Locate every Plasmodium falciparum-infected red blood cell.
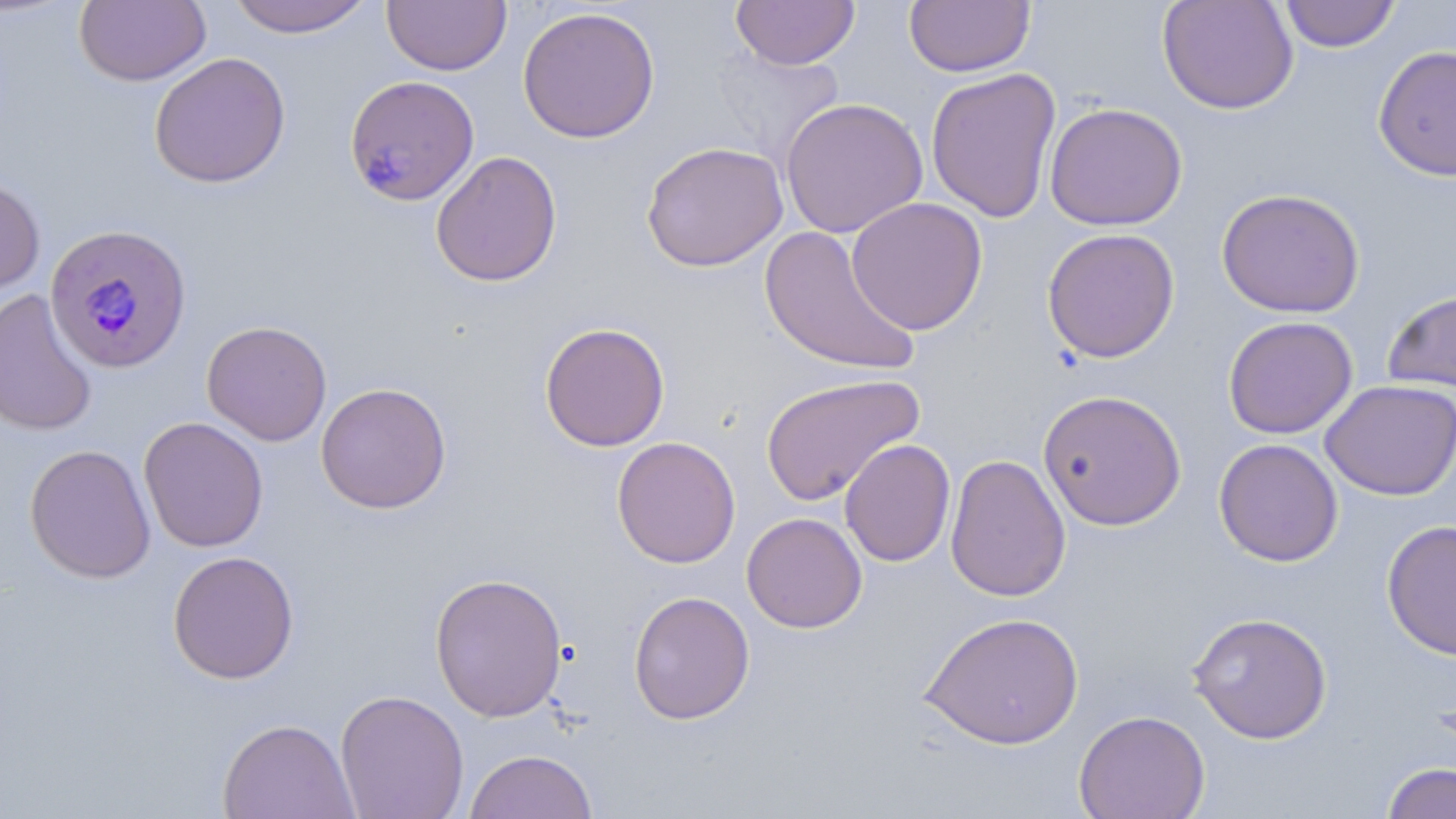
Approximate bounding boxes as (x1, y1, x2, y2) in pixels.
Plasmodium falciparum-infected red blood cells: (344, 75, 480, 206), (42, 225, 190, 374).

Uninfected red blood cell locations: (74, 0, 212, 87), (226, 0, 375, 38), (382, 0, 511, 76), (730, 0, 860, 70), (1157, 0, 1299, 115), (1279, 0, 1401, 52), (904, 1, 1035, 77), (517, 6, 660, 144), (1373, 45, 1456, 181), (148, 52, 292, 188), (925, 66, 1062, 223), (779, 97, 928, 238), (1044, 102, 1188, 231), (641, 140, 789, 272), (430, 150, 563, 288), (0, 174, 46, 296), (1216, 187, 1366, 318), (846, 196, 988, 336), (759, 226, 921, 378), (1041, 228, 1180, 363), (1382, 286, 1456, 395), (0, 289, 99, 436), (1223, 315, 1358, 439), (201, 320, 333, 446), (539, 321, 671, 452), (760, 372, 925, 506), (1320, 379, 1456, 501), (316, 382, 452, 513), (1038, 389, 1187, 531), (138, 416, 269, 553), (612, 436, 741, 569), (1214, 438, 1343, 567), (840, 439, 956, 567), (24, 444, 157, 584), (944, 453, 1072, 603), (742, 512, 868, 633), (1382, 519, 1456, 661), (167, 550, 300, 685), (429, 572, 568, 722), (628, 591, 755, 725), (919, 611, 1085, 750), (1187, 611, 1333, 744), (335, 689, 469, 819), (1073, 709, 1211, 819), (216, 717, 360, 819), (463, 750, 598, 819), (1382, 762, 1456, 819). Slide-level diagnosis: Plasmodium falciparum. Image is 1456×819 pixels. One field of a larger specimen. Light microscopy. May-Grünwald-Giemsa stain. Thin blood smear. 1000x magnification.